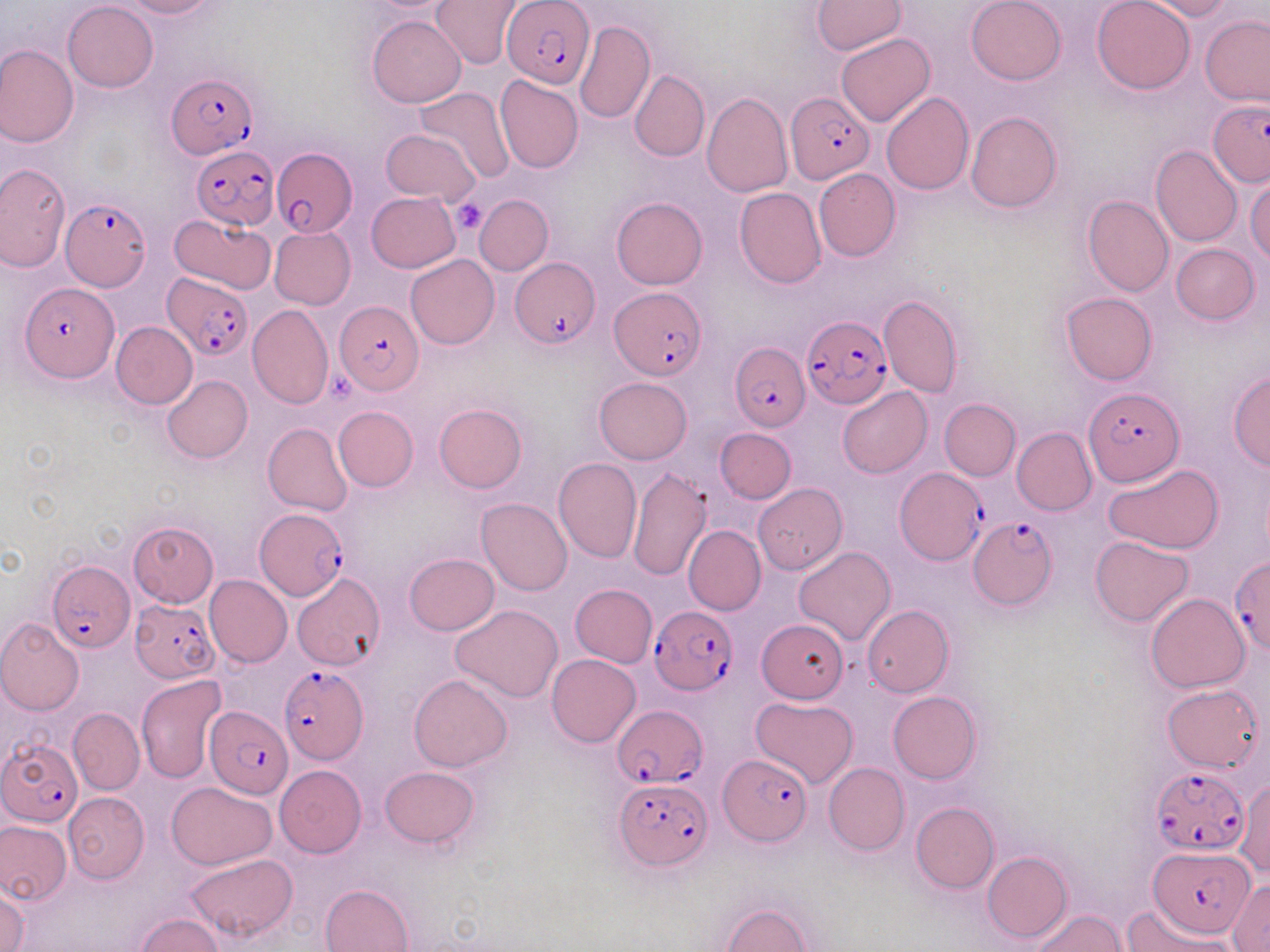 Approximate bounding boxes as named x1/y1/x2/y2 corners in pixels. Platelet locations: (x1=450, y1=196, x2=488, y2=234), (x1=329, y1=372, x2=361, y2=402). Uninfected red blood cell locations (subset): (x1=118, y1=0, x2=215, y2=19), (x1=433, y1=0, x2=524, y2=70), (x1=966, y1=0, x2=1066, y2=85), (x1=1091, y1=0, x2=1195, y2=94), (x1=1147, y1=0, x2=1235, y2=20), (x1=63, y1=1, x2=158, y2=92), (x1=813, y1=1, x2=906, y2=55), (x1=10, y1=12, x2=146, y2=119), (x1=369, y1=15, x2=466, y2=106), (x1=1201, y1=15, x2=1270, y2=105), (x1=574, y1=20, x2=655, y2=124), (x1=836, y1=34, x2=934, y2=126), (x1=0, y1=43, x2=79, y2=147), (x1=629, y1=69, x2=710, y2=162), (x1=494, y1=74, x2=584, y2=174), (x1=416, y1=87, x2=514, y2=183), (x1=701, y1=92, x2=793, y2=198), (x1=881, y1=93, x2=973, y2=195), (x1=966, y1=111, x2=1061, y2=213), (x1=381, y1=128, x2=480, y2=203), (x1=1151, y1=144, x2=1242, y2=247), (x1=0, y1=162, x2=70, y2=273), (x1=814, y1=169, x2=901, y2=261), (x1=1246, y1=178, x2=1270, y2=263), (x1=734, y1=187, x2=827, y2=289), (x1=366, y1=192, x2=461, y2=273), (x1=612, y1=196, x2=708, y2=289), (x1=1083, y1=196, x2=1174, y2=296), (x1=171, y1=213, x2=276, y2=295), (x1=270, y1=226, x2=356, y2=309), (x1=1171, y1=243, x2=1259, y2=324), (x1=406, y1=254, x2=498, y2=349), (x1=1060, y1=292, x2=1157, y2=385), (x1=878, y1=293, x2=964, y2=397), (x1=247, y1=304, x2=334, y2=409), (x1=112, y1=321, x2=197, y2=408), (x1=1228, y1=371, x2=1269, y2=470), (x1=162, y1=374, x2=253, y2=462), (x1=594, y1=377, x2=692, y2=463), (x1=838, y1=387, x2=931, y2=479), (x1=939, y1=399, x2=1021, y2=480), (x1=434, y1=403, x2=528, y2=493), (x1=334, y1=405, x2=419, y2=492), (x1=263, y1=423, x2=353, y2=516), (x1=1011, y1=427, x2=1096, y2=515), (x1=715, y1=428, x2=796, y2=503), (x1=553, y1=458, x2=642, y2=564), (x1=1105, y1=464, x2=1225, y2=554), (x1=626, y1=466, x2=714, y2=580), (x1=753, y1=484, x2=846, y2=573), (x1=476, y1=498, x2=572, y2=595), (x1=127, y1=521, x2=219, y2=608), (x1=684, y1=524, x2=765, y2=615), (x1=1089, y1=536, x2=1194, y2=627), (x1=794, y1=547, x2=896, y2=646), (x1=404, y1=553, x2=499, y2=635), (x1=291, y1=573, x2=385, y2=670), (x1=205, y1=576, x2=292, y2=668), (x1=571, y1=584, x2=657, y2=667), (x1=1147, y1=594, x2=1250, y2=693), (x1=450, y1=604, x2=563, y2=703), (x1=862, y1=604, x2=953, y2=697), (x1=0, y1=617, x2=84, y2=715), (x1=755, y1=618, x2=847, y2=703), (x1=548, y1=654, x2=641, y2=747), (x1=136, y1=674, x2=228, y2=784), (x1=409, y1=675, x2=512, y2=772), (x1=1162, y1=684, x2=1262, y2=772), (x1=888, y1=691, x2=981, y2=784), (x1=749, y1=696, x2=858, y2=788), (x1=68, y1=707, x2=144, y2=795), (x1=824, y1=762, x2=909, y2=855), (x1=274, y1=765, x2=366, y2=858), (x1=380, y1=767, x2=479, y2=848), (x1=1234, y1=775, x2=1269, y2=880), (x1=165, y1=782, x2=277, y2=869), (x1=63, y1=791, x2=148, y2=882), (x1=911, y1=802, x2=999, y2=893), (x1=0, y1=820, x2=70, y2=905), (x1=983, y1=851, x2=1072, y2=943), (x1=183, y1=853, x2=297, y2=944), (x1=1228, y1=879, x2=1270, y2=950), (x1=320, y1=883, x2=415, y2=952), (x1=0, y1=885, x2=29, y2=952), (x1=1124, y1=902, x2=1232, y2=952), (x1=721, y1=903, x2=814, y2=951), (x1=1029, y1=908, x2=1126, y2=952), (x1=135, y1=914, x2=224, y2=951). Plasmodium falciparum-infected red blood cell locations (subset): (x1=503, y1=0, x2=593, y2=88), (x1=166, y1=72, x2=257, y2=158), (x1=785, y1=91, x2=875, y2=183), (x1=1209, y1=101, x2=1270, y2=185), (x1=190, y1=145, x2=278, y2=229), (x1=271, y1=148, x2=356, y2=237), (x1=61, y1=196, x2=151, y2=295), (x1=512, y1=260, x2=598, y2=348), (x1=162, y1=272, x2=252, y2=360), (x1=19, y1=283, x2=119, y2=384), (x1=610, y1=288, x2=707, y2=380), (x1=333, y1=301, x2=424, y2=395), (x1=801, y1=316, x2=893, y2=409), (x1=730, y1=343, x2=810, y2=431), (x1=1083, y1=387, x2=1184, y2=488), (x1=896, y1=466, x2=985, y2=563), (x1=255, y1=509, x2=348, y2=601), (x1=968, y1=516, x2=1056, y2=609), (x1=1229, y1=558, x2=1270, y2=655), (x1=47, y1=559, x2=133, y2=653), (x1=129, y1=600, x2=220, y2=683), (x1=650, y1=605, x2=736, y2=694), (x1=277, y1=664, x2=368, y2=764), (x1=611, y1=704, x2=707, y2=786), (x1=205, y1=706, x2=292, y2=797), (x1=2, y1=739, x2=81, y2=826), (x1=720, y1=754, x2=811, y2=845), (x1=1149, y1=766, x2=1248, y2=856), (x1=613, y1=776, x2=711, y2=867), (x1=1148, y1=847, x2=1255, y2=938). Slide-level diagnosis: Plasmodium falciparum. Thin blood smear. One field of a larger specimen. May-Grünwald-Giemsa-stained preparation. Optical microscopy. Image is 1270×952 pixels. Captured at 1000x magnification.